Locate platelets.
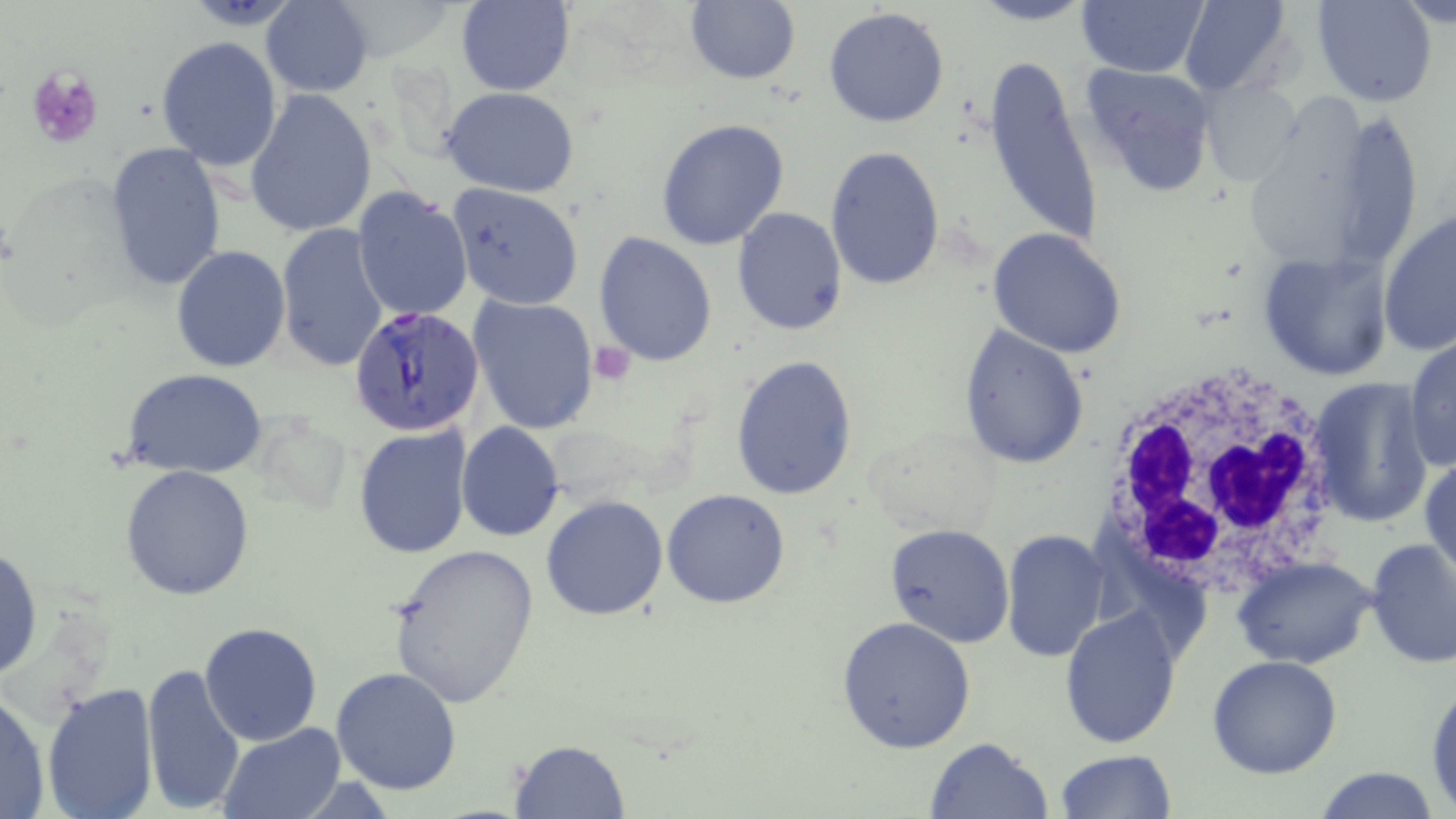

Approximate bounding boxes as (x1,y1)-(x2,y2) corner pairs in pixels.
Platelets: (27,66)-(102,148), (589,340)-(636,382).

slide-level diagnosis = Plasmodium falciparum
field of view = one of a larger specimen
image size = 1456×819 pixels
preparation = thin blood smear
modality = optical microscopy
stain = May-Grünwald-Giemsa
Plasmodium falciparum-infected red blood cell locations = approximate bounding boxes as (x1,y1)-(x2,y2) corner pairs in pixels: (351,305)-(486,432)
magnification = 1000x
uninfected red blood cell locations = approximate bounding boxes as (x1,y1)-(x2,y2) corner pairs in pixels: (973,0)-(1092,26), (1077,0)-(1207,76), (1178,0)-(1295,98), (1309,0)-(1438,107), (261,1)-(373,97), (457,1)-(575,96), (683,2)-(801,85), (824,7)-(951,128), (156,35)-(283,172), (982,53)-(1104,252), (1077,63)-(1220,199), (1197,77)-(1304,188), (441,87)-(582,196), (246,89)-(377,238), (656,118)-(790,251), (103,141)-(227,296), (825,144)-(946,290), (448,184)-(585,310), (351,185)-(473,322), (732,207)-(847,334), (1378,208)-(1456,357), (277,223)-(390,374), (987,228)-(1128,359), (593,232)-(718,368), (171,245)-(290,371), (1257,247)-(1394,381), (468,294)-(600,434), (957,324)-(1090,470), (1404,333)-(1456,474), (730,354)-(859,500), (124,368)-(266,478), (1306,376)-(1434,527), (455,420)-(565,543), (354,424)-(472,559), (1421,451)-(1455,580), (120,463)-(255,600), (661,490)-(790,609), (540,495)-(668,621), (884,523)-(1017,648), (1000,528)-(1108,665), (1365,538)-(1456,668), (386,541)-(541,708), (0,545)-(43,684), (1234,555)-(1378,670), (1059,607)-(1182,748), (837,617)-(977,756), (199,622)-(322,746), (1207,654)-(1342,777), (141,663)-(244,816), (331,668)-(462,796), (1426,678)-(1456,812), (40,682)-(159,819), (0,687)-(51,819), (219,723)-(344,817), (922,735)-(1054,819), (512,739)-(629,817), (1054,750)-(1177,819), (1313,765)-(1441,819)
white blood cell locations = approximate bounding boxes as (x1,y1)-(x2,y2) corner pairs in pixels: (1095,363)-(1344,598)